Classify this cell by malaria status.
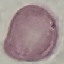

It is uninfected.

{
  "image_type": "automatically extracted cell patch, resized to 64 × 64 pixels",
  "stain": "Giemsa",
  "capture": "smartphone camera at the microscope eyepiece",
  "preparation": "thin smear"
}